Assess the morphology of the erythrocytes.
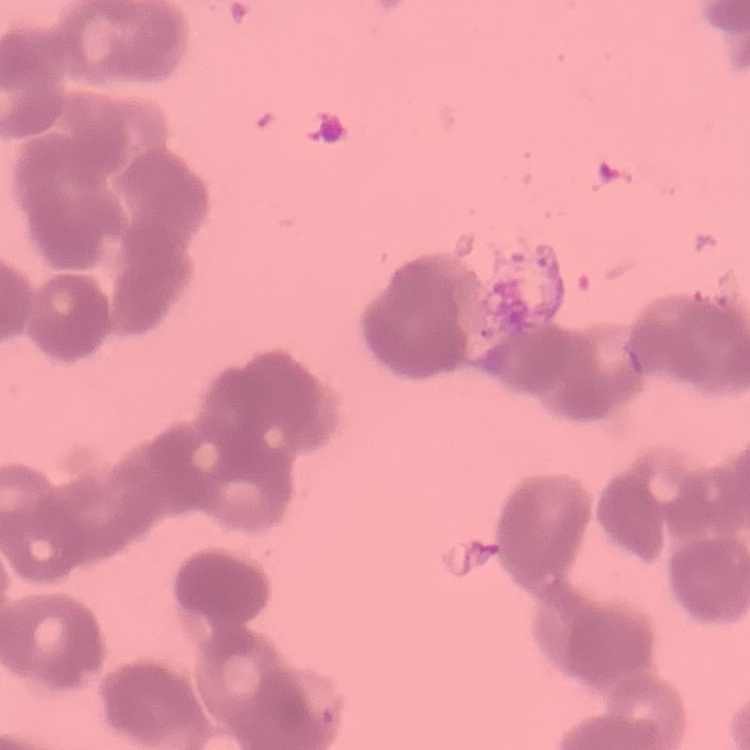

They show rouleaux formation.

image type = one tile cut from a larger photomicrograph
stain = Field's or Giemsa
preparation = thin peripheral smear